Assess the morphology of the erythrocytes.
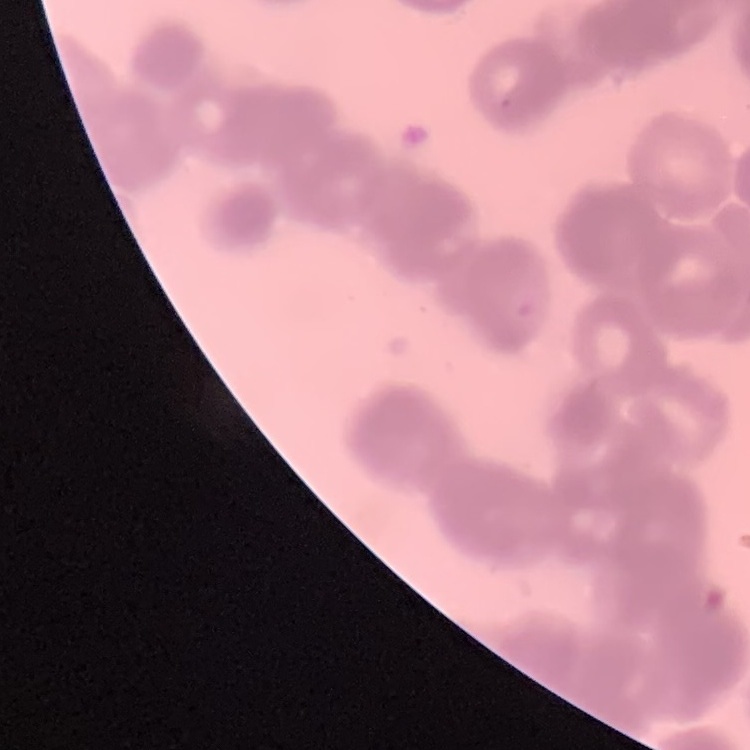
Rouleaux formation.

One tile cut from a larger photomicrograph. Field's or Giemsa stain. Thin blood film.